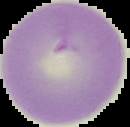
Summary:
  - Image type: segmented cell region on a black background
  - Result: negative for malaria parasites
  - Preparation: thin blood film
  - Image size: 130×127 pixels